Assess this cell for malaria.
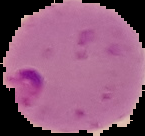

It is parasitized.

preparation: thin blood film
image_size: 145×136 pixels
image_type: cell region segmented out of the field of view; surrounding area masked to black